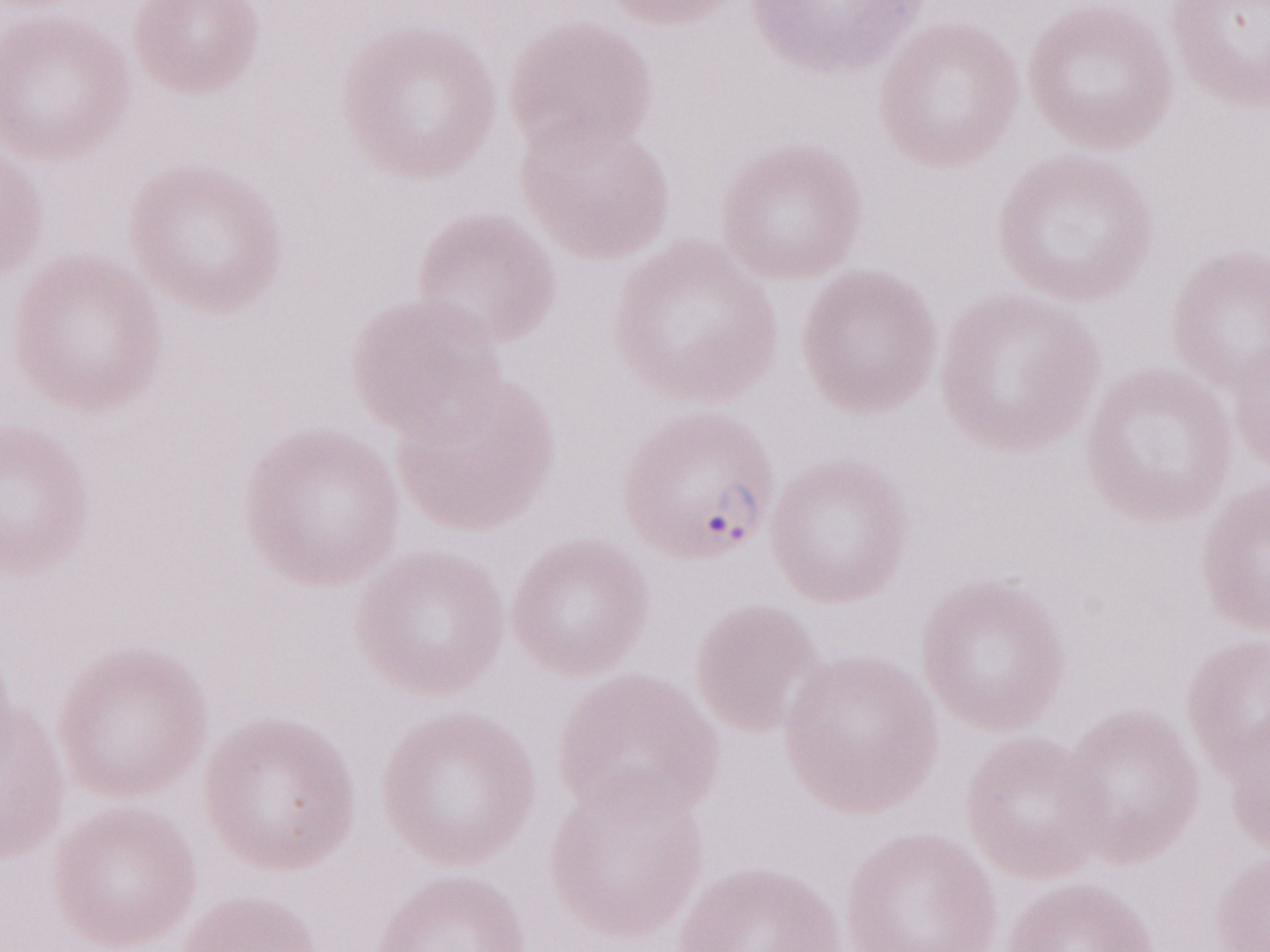
May-Grünwald-Giemsa-stained preparation. Thin blood smear. Image is 1270×952 pixels. Olympus BX43 microscope, Olympus DP73 camera. 1,000x magnification. Single field of view. Patient-level malaria diagnosis: positive.